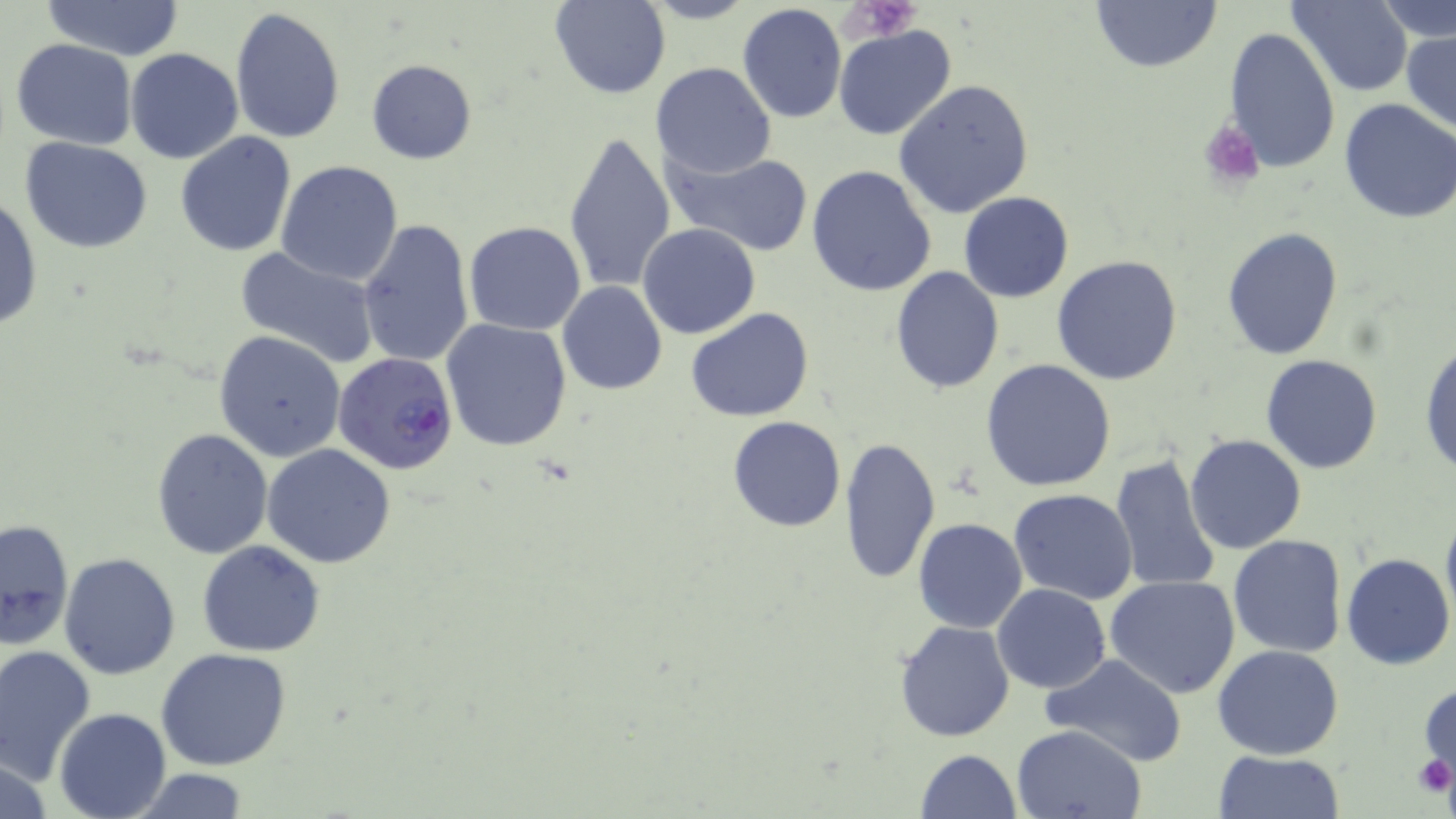 Approximate bounding boxes as (x1,y1)-(x2,y2) corner pairs in pixels. Plasmodium falciparum-infected red blood cell locations: (333,352)-(458,477). Platelet locations: (845,0)-(921,41), (1198,117)-(1266,190), (1413,753)-(1455,798). Uninfected red blood cell locations: (638,0)-(758,26), (1088,0)-(1223,74), (1292,0)-(1412,96), (41,1)-(186,60), (549,1)-(671,100), (1381,1)-(1456,45), (736,3)-(848,125), (228,6)-(345,145), (833,24)-(957,140), (1224,27)-(1341,172), (1400,30)-(1456,135), (10,39)-(138,150), (126,48)-(243,164), (366,59)-(478,165), (651,62)-(776,178), (893,80)-(1035,219), (1336,98)-(1456,224), (563,129)-(677,296), (176,130)-(297,256), (21,137)-(153,254), (663,149)-(815,256), (274,160)-(403,285), (806,164)-(937,299), (958,192)-(1074,302), (0,193)-(42,333), (357,216)-(474,368), (463,221)-(586,335), (638,223)-(761,338), (1222,227)-(1343,360), (234,245)-(381,364), (1052,256)-(1183,387), (892,265)-(1005,394), (557,281)-(667,397), (687,307)-(815,422), (439,318)-(571,452), (214,331)-(346,461), (1419,337)-(1456,479), (1261,354)-(1384,475), (981,358)-(1116,491), (726,415)-(848,532), (151,429)-(272,558), (1186,433)-(1307,553), (839,434)-(941,586), (263,444)-(397,568), (1108,454)-(1223,595), (1009,489)-(1139,605), (1440,505)-(1456,635), (1,517)-(73,648), (913,518)-(1027,634), (1227,535)-(1348,658), (185,539)-(317,769), (196,540)-(326,657), (59,553)-(181,678), (1340,553)-(1455,670), (1105,574)-(1241,698), (993,583)-(1110,694), (895,619)-(1015,740), (1213,644)-(1344,760), (0,645)-(97,781), (156,647)-(294,771), (1043,656)-(1188,766), (1419,679)-(1456,787), (55,708)-(171,819), (1013,724)-(1145,818), (0,749)-(55,819), (915,749)-(1021,819), (1210,750)-(1347,818), (120,769)-(257,819). Slide-level diagnosis: Plasmodium falciparum. May-Grünwald-Giemsa-stained preparation. Image is 1456×819 pixels. Light microscopy. Captured at 1000x magnification. Single field of view. Thin blood film.